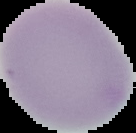

image type = cell region segmented out of the field of view; surrounding area masked to black
preparation = thin blood smear
result = no Plasmodium parasites seen
image size = 136×133 pixels